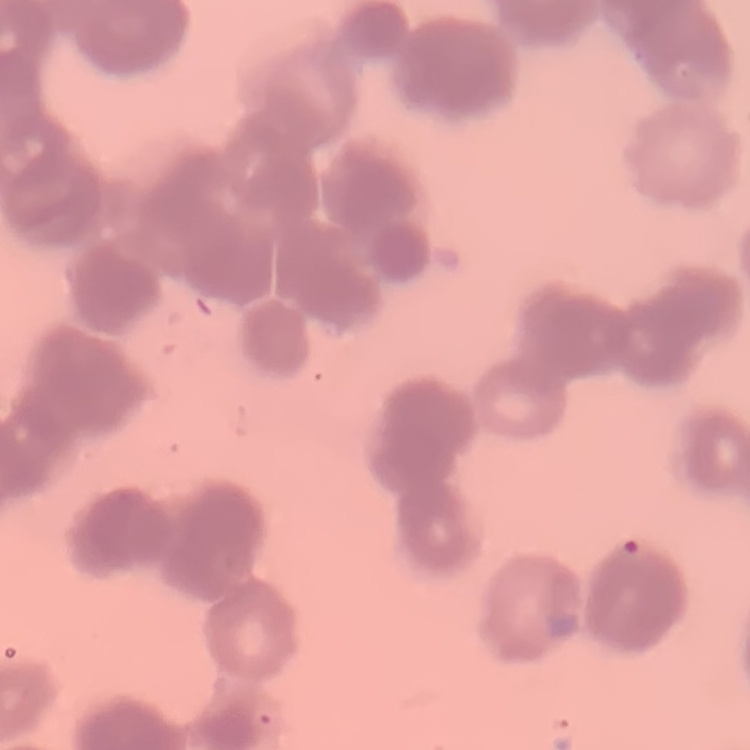 The erythrocytes show rouleaux formation. Field's or Giemsa stain. Thin blood film. Square crop of a larger photomicrograph.